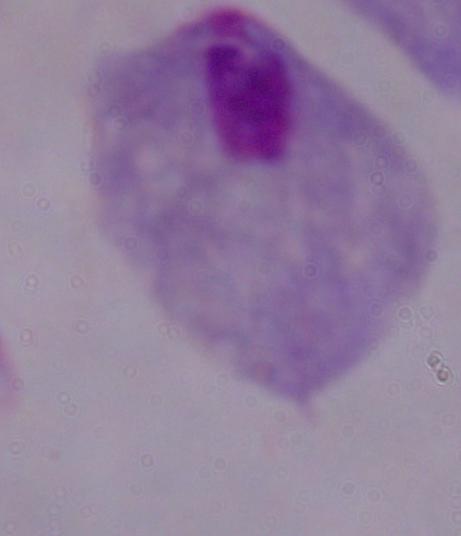
modality = photomicrograph
magnification = 1000x
identification = trichomonad